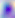

Summary:
  - Modality: photomicrograph
  - Identification: Toxoplasma gondii
  - Magnification: 400x